Classify this cell by malaria status.
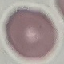

It is uninfected.

Automatically extracted cell patch, resized to 64 × 64 pixels. Photographed with a smartphone camera at the microscope eyepiece. Giemsa stain. Thin blood smear.